Report the malaria status of this cell.
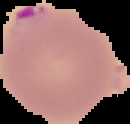

It is parasitized.

preparation = thin blood smear
image size = 130×124 pixels
image type = cell region segmented out of the field of view; surrounding area masked to black